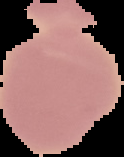

Summary:
  - Preparation: thin blood film
  - Result: no malaria parasites seen
  - Image size: 124×157 pixels
  - Image type: cell region segmented out of the field of view; surrounding area masked to black